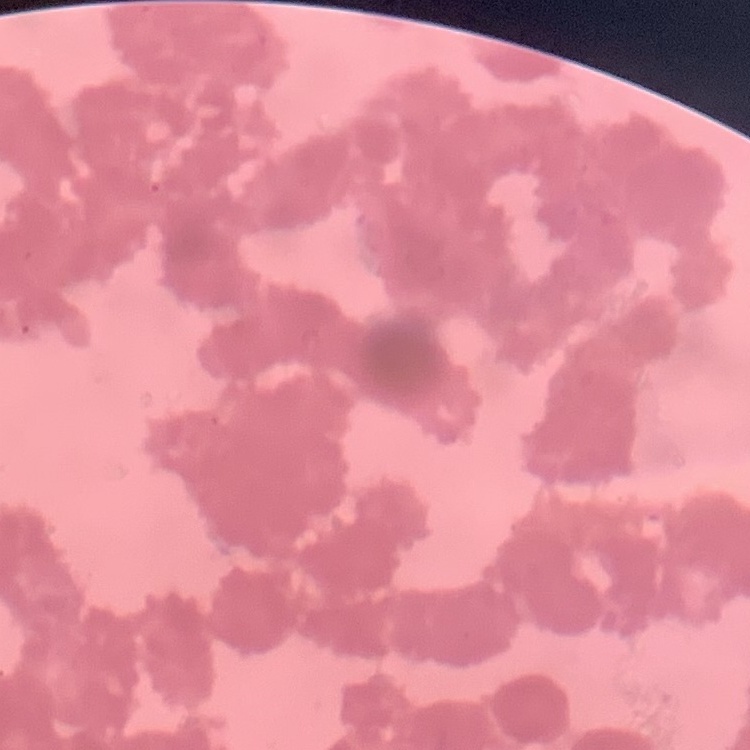

red blood cell morphology = rouleaux formation
image type = one tile cut from a larger photomicrograph
preparation = thin blood smear
stain = Field's or Giemsa